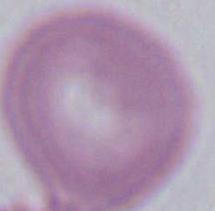
Summary:
  - Identification: red blood cell
  - Modality: micrograph
  - Magnification: 1000x